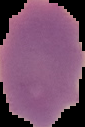
Image is 85×127 pixels. From a thin blood film. Result: no malaria parasites detected. Cell region segmented out of the field of view; the surrounding area is masked to black.